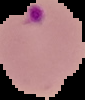

image size = 85×100 pixels
malaria status = parasitized
image type = segmented cell region on a black background
preparation = thin blood smear